Comment on the morphology of the red blood cells.
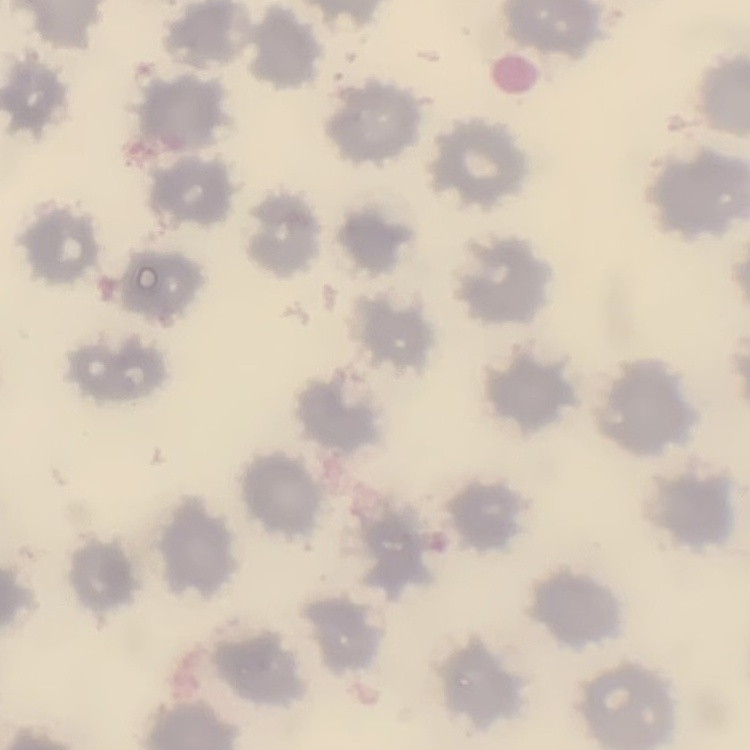
They show no rouleaux formation.

preparation = thin blood film
image type = one tile cut from a larger photomicrograph
stain = Field's or Giemsa